Evaluate for malaria.
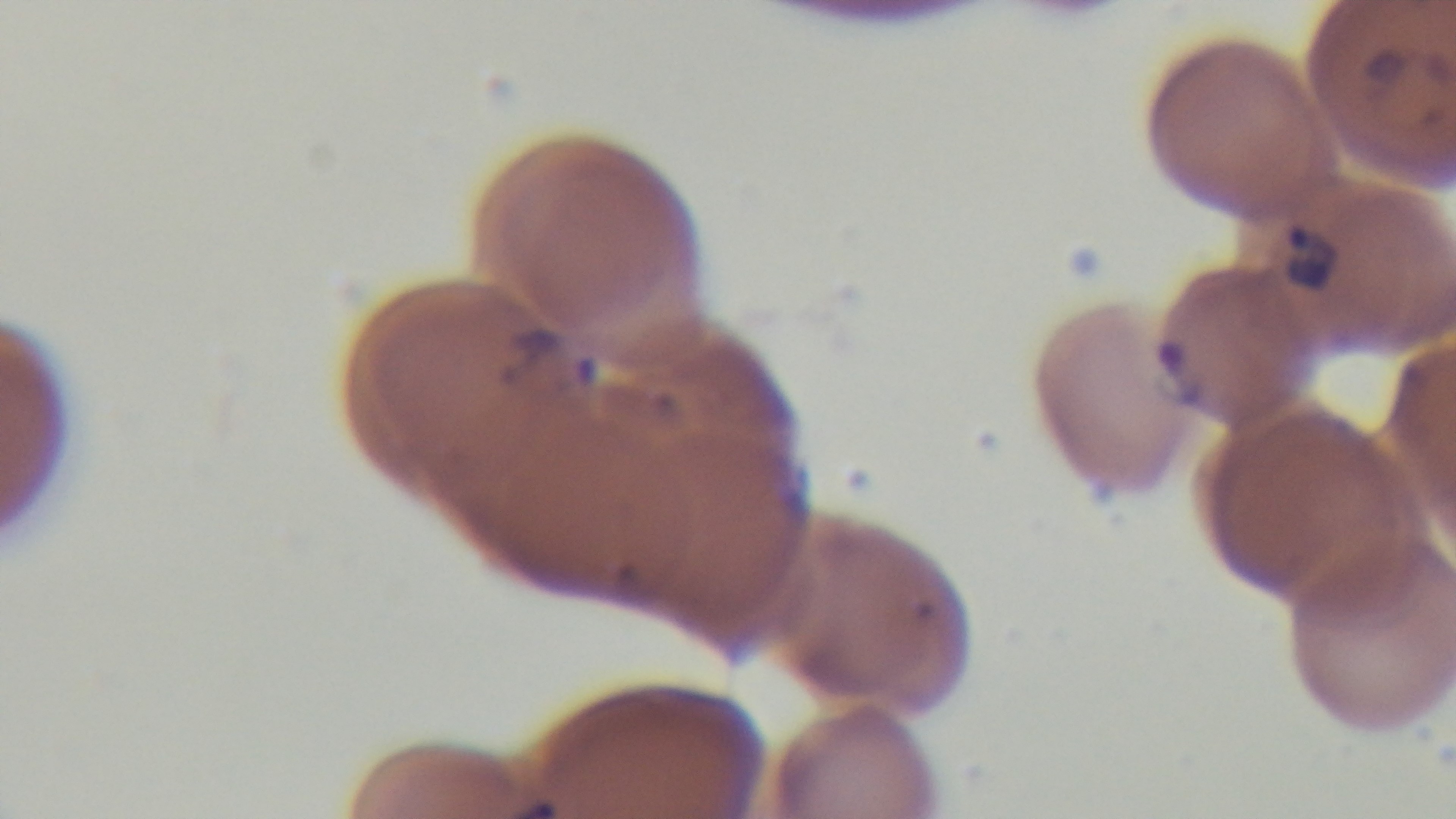
Positive.

Summary:
  - Objective: 100x oil immersion
  - Capture: mounted 4K digital camera
  - Preparation: thin
  - Field of view: single
  - Modality: light microscopy
  - Stain: Giemsa